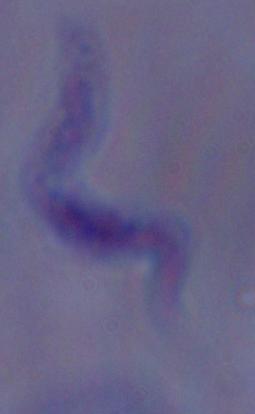

Summary:
  - Magnification: 1000x
  - Identification: trypanosome
  - Modality: photomicrograph